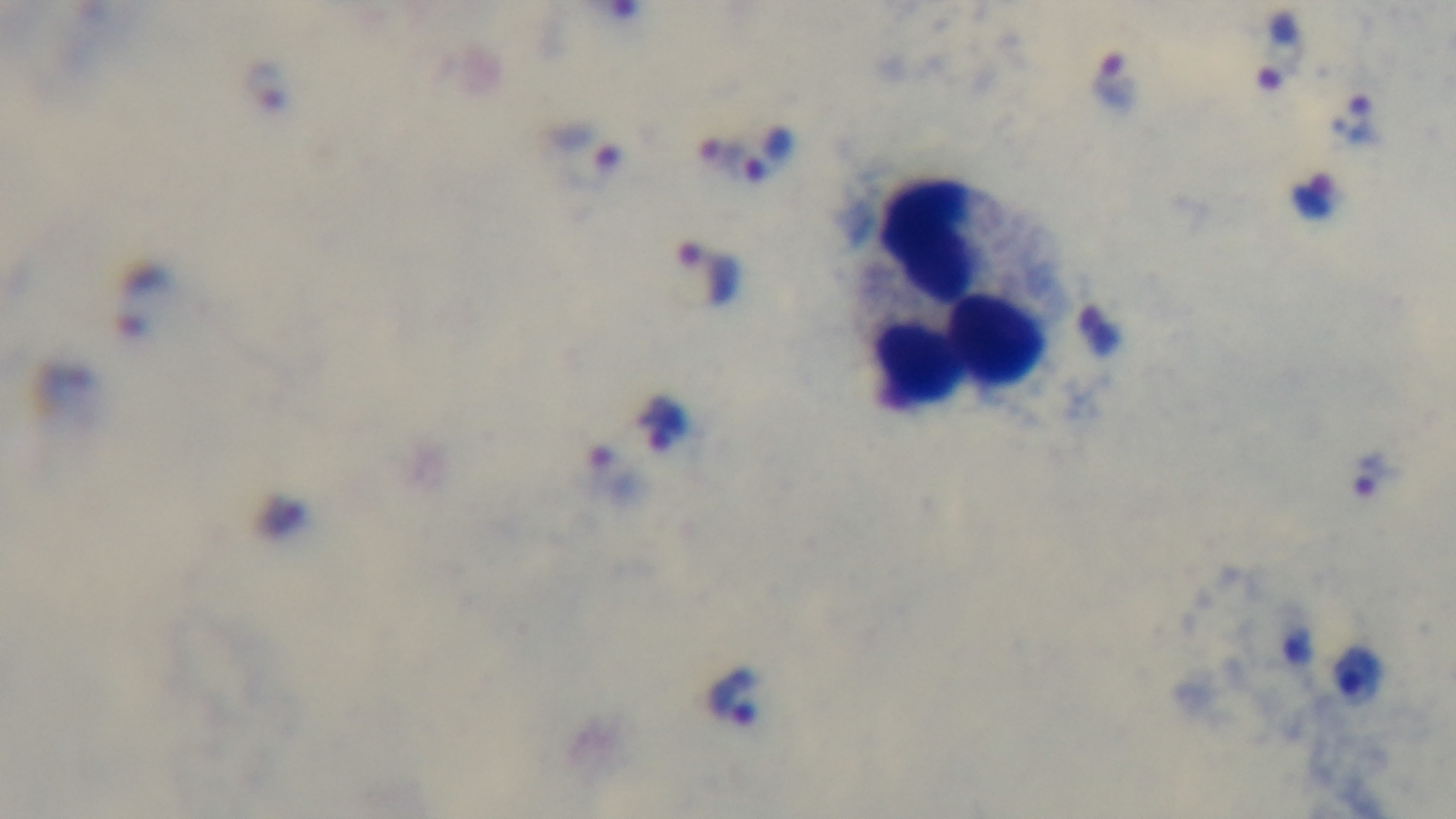

{
  "modality": "light microscopy",
  "capture": "mounted 4K digital camera",
  "stain": "Giemsa",
  "objective": "100x oil immersion",
  "preparation": "thick",
  "field_of_view": "one from the slide",
  "malaria_status": "positive"
}